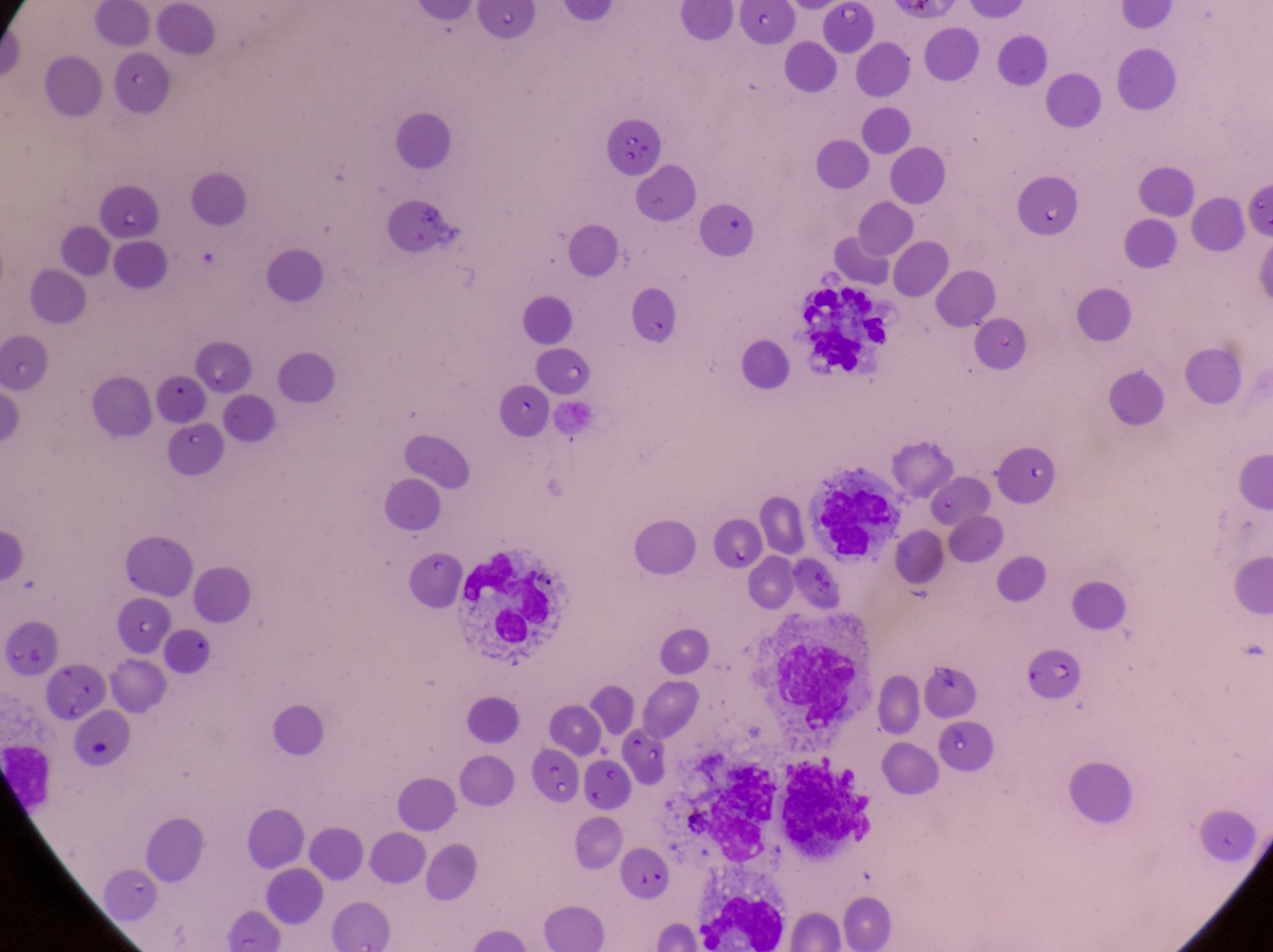

leukocyte locations = approximate bounding boxes as {left, top, right, bottom} in pixels: {800, 280, 894, 380}, {813, 478, 902, 563}, {460, 545, 568, 657}, {780, 641, 859, 733}, {689, 749, 774, 862}, {780, 755, 888, 854}, {698, 877, 786, 944}
artifact (platelet-like body, stain precipitate, or debris) locations = approximate bounding boxes as {left, top, right, bottom} in pixels: {534, 742, 579, 804}, {586, 754, 631, 814}
image size = 1273×952 pixels
capture = smartphone photograph through the eyepiece of an Olympus CX-23 microscope
preparation = thin blood film
field of view = single
magnification = 1000x
country = Uganda
parasitised red blood cell locations = approximate bounding boxes as {left, top, right, bottom} in pixels: {606, 110, 661, 173}, {1025, 642, 1090, 705}